Describe the morphology of the red blood cells.
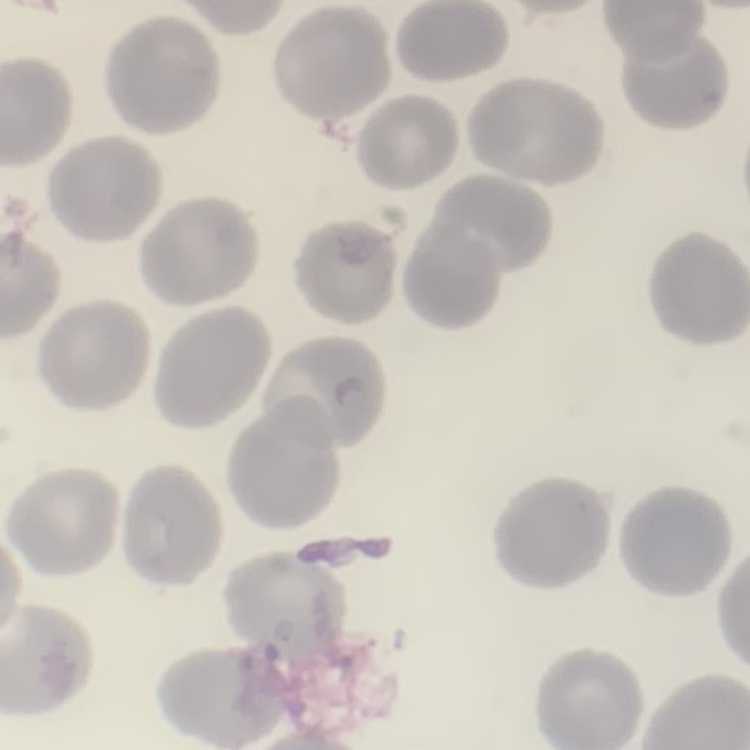
No rouleaux formation.

stain = Field's or Giemsa
image type = one tile cut from a larger photomicrograph
preparation = thin blood smear